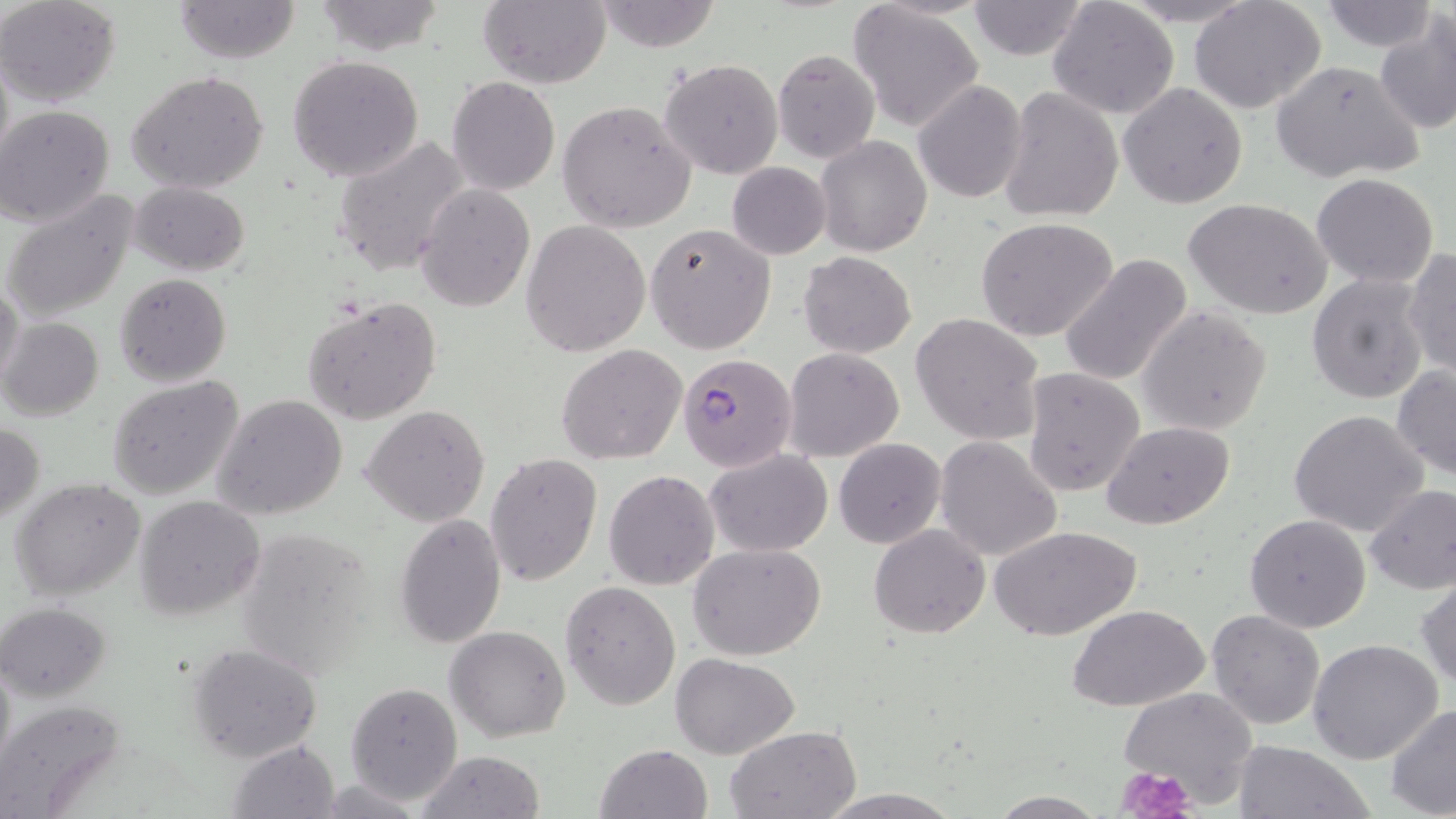

Approximate bounding boxes as named x1/y1/x2/y2 corners in pixels. Plasmodium falciparum-infected red blood cell locations: (x1=679, y1=353, x2=797, y2=470). Uninfected red blood cell locations: (x1=0, y1=0, x2=122, y2=106), (x1=175, y1=0, x2=302, y2=64), (x1=311, y1=0, x2=446, y2=55), (x1=1321, y1=0, x2=1433, y2=50), (x1=475, y1=1, x2=612, y2=88), (x1=595, y1=1, x2=720, y2=52), (x1=1191, y1=1, x2=1328, y2=114), (x1=964, y1=2, x2=1092, y2=61), (x1=1048, y1=3, x2=1176, y2=119), (x1=849, y1=5, x2=986, y2=132), (x1=1376, y1=13, x2=1456, y2=135), (x1=771, y1=47, x2=880, y2=163), (x1=286, y1=54, x2=424, y2=181), (x1=658, y1=58, x2=784, y2=181), (x1=1268, y1=59, x2=1425, y2=183), (x1=127, y1=69, x2=270, y2=194), (x1=447, y1=75, x2=560, y2=194), (x1=912, y1=80, x2=1028, y2=203), (x1=1119, y1=82, x2=1248, y2=208), (x1=999, y1=86, x2=1125, y2=224), (x1=558, y1=99, x2=697, y2=233), (x1=2, y1=105, x2=116, y2=228), (x1=332, y1=135, x2=471, y2=276), (x1=817, y1=135, x2=931, y2=256), (x1=727, y1=162, x2=832, y2=260), (x1=1312, y1=174, x2=1439, y2=288), (x1=131, y1=181, x2=250, y2=275), (x1=416, y1=184, x2=536, y2=311), (x1=3, y1=188, x2=139, y2=322), (x1=1186, y1=200, x2=1332, y2=319), (x1=975, y1=216, x2=1119, y2=342), (x1=521, y1=221, x2=651, y2=357), (x1=646, y1=221, x2=777, y2=355), (x1=1403, y1=249, x2=1455, y2=379), (x1=799, y1=251, x2=916, y2=357), (x1=1058, y1=254, x2=1195, y2=387), (x1=115, y1=273, x2=231, y2=386), (x1=1307, y1=273, x2=1429, y2=404), (x1=0, y1=281, x2=24, y2=393), (x1=303, y1=299, x2=442, y2=424), (x1=1138, y1=306, x2=1273, y2=435), (x1=910, y1=313, x2=1045, y2=446), (x1=0, y1=317, x2=103, y2=422), (x1=556, y1=343, x2=687, y2=465), (x1=784, y1=347, x2=903, y2=461), (x1=1392, y1=364, x2=1456, y2=481), (x1=1023, y1=367, x2=1146, y2=496), (x1=106, y1=375, x2=245, y2=500), (x1=213, y1=394, x2=348, y2=521), (x1=361, y1=404, x2=490, y2=527), (x1=1288, y1=410, x2=1429, y2=537), (x1=1102, y1=421, x2=1234, y2=531), (x1=1, y1=423, x2=45, y2=523), (x1=935, y1=437, x2=1063, y2=562), (x1=833, y1=438, x2=945, y2=549), (x1=705, y1=449, x2=833, y2=557), (x1=483, y1=452, x2=602, y2=588), (x1=605, y1=470, x2=720, y2=591), (x1=11, y1=477, x2=147, y2=602), (x1=1362, y1=484, x2=1456, y2=596), (x1=135, y1=494, x2=265, y2=620), (x1=394, y1=513, x2=506, y2=648), (x1=1245, y1=514, x2=1371, y2=633), (x1=869, y1=524, x2=990, y2=638), (x1=234, y1=525, x2=381, y2=681), (x1=992, y1=527, x2=1139, y2=642), (x1=688, y1=544, x2=826, y2=661), (x1=1415, y1=573, x2=1456, y2=692), (x1=561, y1=582, x2=681, y2=710), (x1=2, y1=601, x2=115, y2=702), (x1=1069, y1=605, x2=1208, y2=713), (x1=1207, y1=611, x2=1326, y2=730), (x1=444, y1=625, x2=571, y2=742), (x1=377, y1=633, x2=521, y2=773), (x1=1306, y1=639, x2=1444, y2=764), (x1=186, y1=643, x2=323, y2=763), (x1=672, y1=654, x2=800, y2=759), (x1=346, y1=681, x2=462, y2=805), (x1=1117, y1=686, x2=1260, y2=808), (x1=0, y1=699, x2=125, y2=817), (x1=1385, y1=704, x2=1456, y2=818), (x1=726, y1=725, x2=859, y2=817), (x1=226, y1=739, x2=340, y2=817), (x1=1232, y1=740, x2=1376, y2=819), (x1=593, y1=744, x2=712, y2=819), (x1=414, y1=751, x2=546, y2=819), (x1=815, y1=789, x2=963, y2=819), (x1=988, y1=792, x2=1109, y2=817). Platelet locations: (x1=1117, y1=763, x2=1198, y2=819). Slide-level diagnosis: Plasmodium falciparum. May-Grünwald-Giemsa-stained preparation. Light microscopy. Single field of view. Image is 1456×819 pixels. 1000x magnification. Thin blood smear.